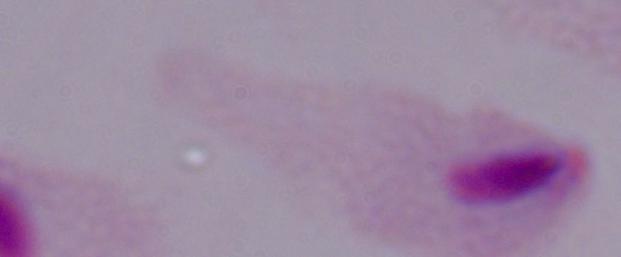

Summary:
  - Magnification: 1000x
  - Identification: trichomonad
  - Modality: photomicrograph